Report the malaria status of this cell.
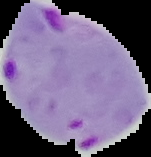

Parasitized.

{
  "image_size": "151×157 pixels",
  "preparation": "thin blood smear",
  "image_type": "cell region segmented out of the field of view; surrounding area masked to black"
}